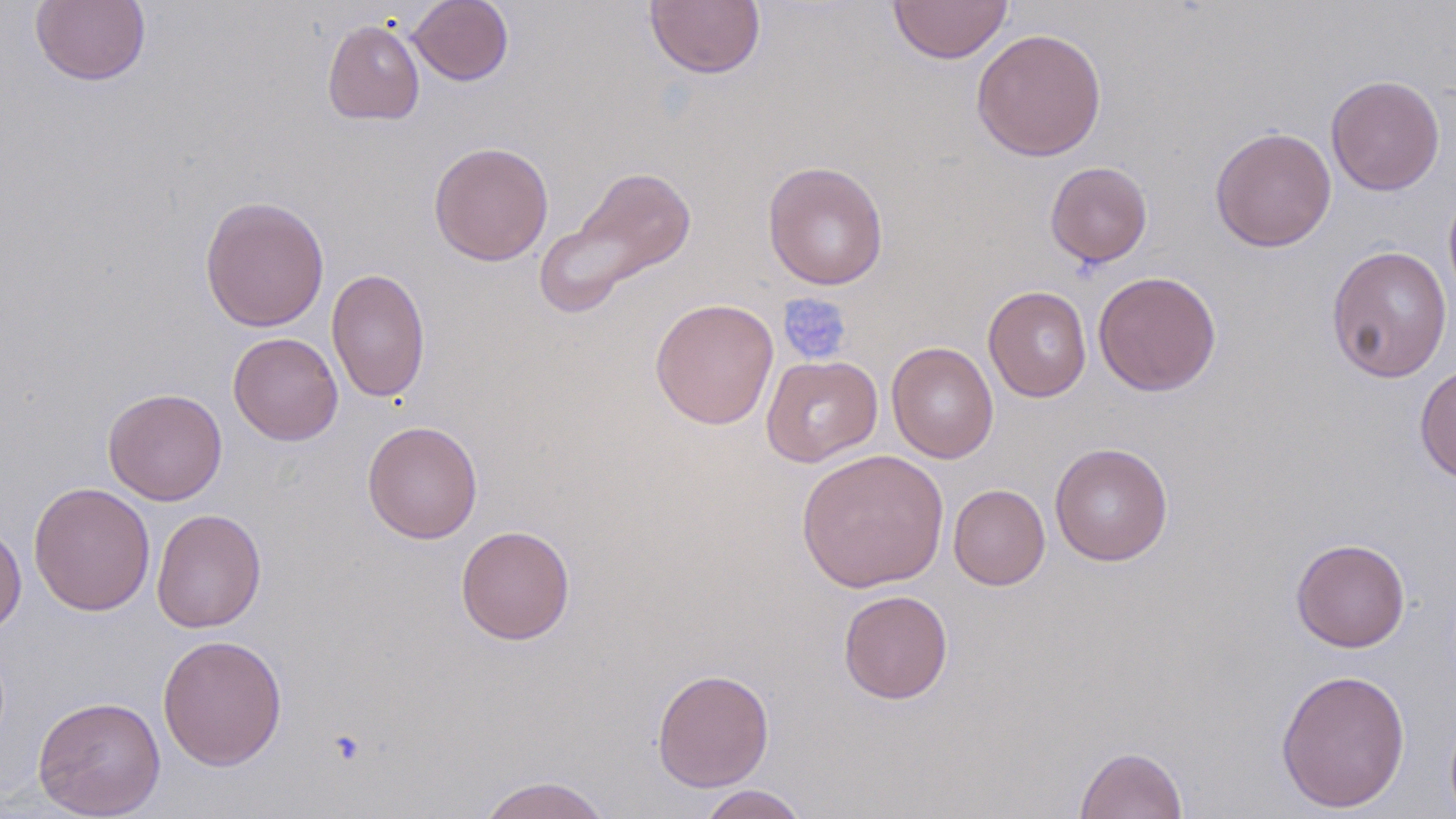

Summary:
  - Coordinate format: approximate bounding boxes as (x1,y1)-(x2,y2) corner pairs in pixels
  - Uninfected red blood cell locations: (30,0)-(151,87), (408,0)-(514,86), (644,1)-(766,80), (888,1)-(1014,64), (322,19)-(424,125), (971,27)-(1107,162), (1326,75)-(1445,196), (1210,127)-(1337,252), (428,141)-(554,266), (763,160)-(889,291), (1045,161)-(1153,268), (538,165)-(698,313), (1443,182)-(1456,309), (199,195)-(330,332), (1326,245)-(1453,382), (326,267)-(430,404), (1093,271)-(1221,396), (983,286)-(1092,402), (650,298)-(779,430), (229,333)-(343,445), (887,342)-(999,462), (761,354)-(883,467), (1414,362)-(1456,484), (103,388)-(227,505), (362,420)-(483,544), (1050,442)-(1173,566), (796,449)-(949,593), (28,482)-(155,616), (948,484)-(1050,590), (151,508)-(267,634), (0,522)-(27,636), (456,524)-(575,645), (1291,538)-(1410,652), (838,589)-(953,704), (157,634)-(288,771), (652,668)-(774,791), (1275,668)-(1411,813), (33,696)-(165,818), (1075,745)-(1188,819), (475,774)-(614,819), (696,785)-(808,819)
  - Platelet locations: (778,293)-(852,366)
  - Slide-level diagnosis: negative for blood parasites
  - Modality: light microscopy
  - Preparation: thin blood film
  - Magnification: 1000x
  - Image size: 1456×819 pixels
  - Stain: May-Grünwald-Giemsa
  - Field of view: one of a larger specimen